Identify the blood parasite species.
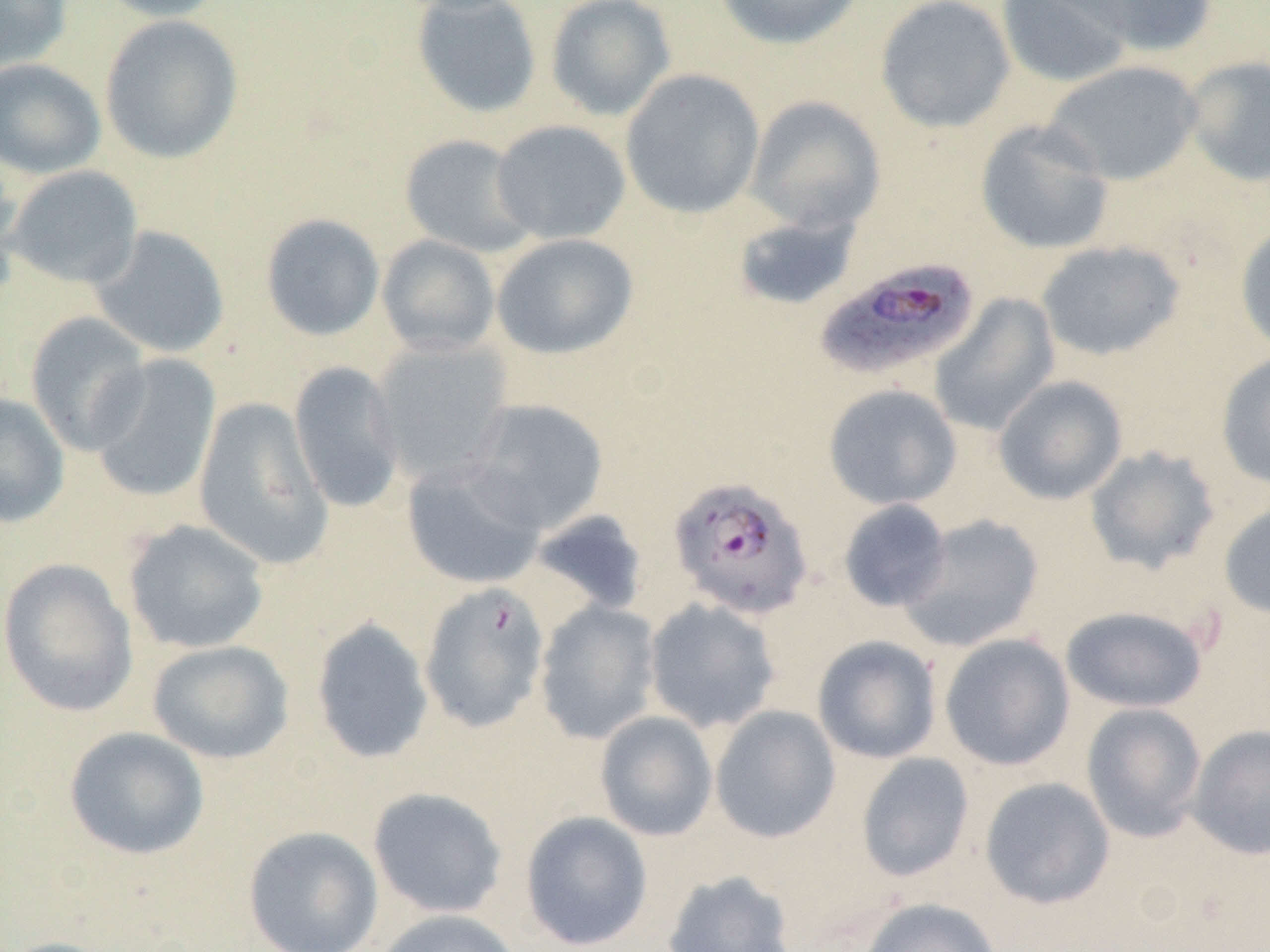

Plasmodium falciparum.

Approximate bounding boxes as named x1/y1/x2/y2 corners in pixels. Uninfected red blood cell locations: (x1=0, y1=0, x2=72, y2=72), (x1=93, y1=0, x2=229, y2=22), (x1=411, y1=0, x2=542, y2=119), (x1=544, y1=0, x2=677, y2=121), (x1=713, y1=0, x2=865, y2=50), (x1=875, y1=0, x2=1016, y2=133), (x1=995, y1=0, x2=1133, y2=89), (x1=1057, y1=0, x2=1219, y2=58), (x1=99, y1=14, x2=243, y2=165), (x1=1182, y1=55, x2=1270, y2=187), (x1=0, y1=58, x2=106, y2=179), (x1=1043, y1=60, x2=1203, y2=186), (x1=620, y1=68, x2=765, y2=220), (x1=745, y1=95, x2=886, y2=234), (x1=490, y1=119, x2=631, y2=244), (x1=975, y1=119, x2=1115, y2=255), (x1=399, y1=133, x2=539, y2=257), (x1=0, y1=155, x2=24, y2=302), (x1=6, y1=165, x2=143, y2=289), (x1=731, y1=211, x2=861, y2=312), (x1=260, y1=213, x2=385, y2=341), (x1=1235, y1=222, x2=1270, y2=356), (x1=89, y1=225, x2=231, y2=359), (x1=491, y1=233, x2=639, y2=360), (x1=376, y1=234, x2=501, y2=357), (x1=1035, y1=240, x2=1185, y2=361), (x1=929, y1=293, x2=1061, y2=436), (x1=25, y1=311, x2=153, y2=455), (x1=369, y1=338, x2=514, y2=482), (x1=1216, y1=350, x2=1270, y2=491), (x1=87, y1=354, x2=221, y2=504), (x1=288, y1=360, x2=407, y2=513), (x1=993, y1=375, x2=1128, y2=505), (x1=823, y1=384, x2=962, y2=511), (x1=0, y1=393, x2=70, y2=528), (x1=193, y1=397, x2=333, y2=570), (x1=464, y1=398, x2=608, y2=534), (x1=1083, y1=445, x2=1221, y2=574), (x1=401, y1=457, x2=547, y2=589), (x1=838, y1=499, x2=951, y2=612), (x1=1218, y1=500, x2=1270, y2=619), (x1=530, y1=509, x2=650, y2=616), (x1=897, y1=513, x2=1044, y2=652), (x1=122, y1=519, x2=270, y2=654), (x1=0, y1=558, x2=139, y2=718), (x1=643, y1=598, x2=782, y2=734), (x1=534, y1=600, x2=662, y2=744), (x1=1060, y1=605, x2=1208, y2=713), (x1=310, y1=617, x2=434, y2=765), (x1=938, y1=633, x2=1075, y2=771), (x1=812, y1=635, x2=943, y2=764), (x1=146, y1=640, x2=294, y2=765), (x1=1080, y1=702, x2=1208, y2=842), (x1=709, y1=705, x2=841, y2=843), (x1=594, y1=710, x2=718, y2=841), (x1=1187, y1=724, x2=1270, y2=861), (x1=64, y1=726, x2=210, y2=860), (x1=855, y1=752, x2=975, y2=882), (x1=979, y1=776, x2=1116, y2=910), (x1=367, y1=786, x2=508, y2=919), (x1=520, y1=811, x2=653, y2=950), (x1=242, y1=825, x2=384, y2=952), (x1=661, y1=869, x2=798, y2=952), (x1=858, y1=896, x2=1002, y2=952), (x1=372, y1=908, x2=524, y2=952), (x1=0, y1=936, x2=123, y2=952). Plasmodium falciparum-infected red blood cell locations: (x1=815, y1=256, x2=981, y2=382), (x1=667, y1=475, x2=814, y2=619), (x1=418, y1=581, x2=550, y2=734). One field of a larger specimen. 1000x magnification. Thin blood smear. Image is 1270×952 pixels. Optical microscopy.